Assess this cell for malaria.
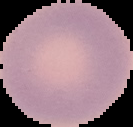
Uninfected.

preparation: thin blood film
image_size: 133×127 pixels
image_type: segmented cell region on a black background